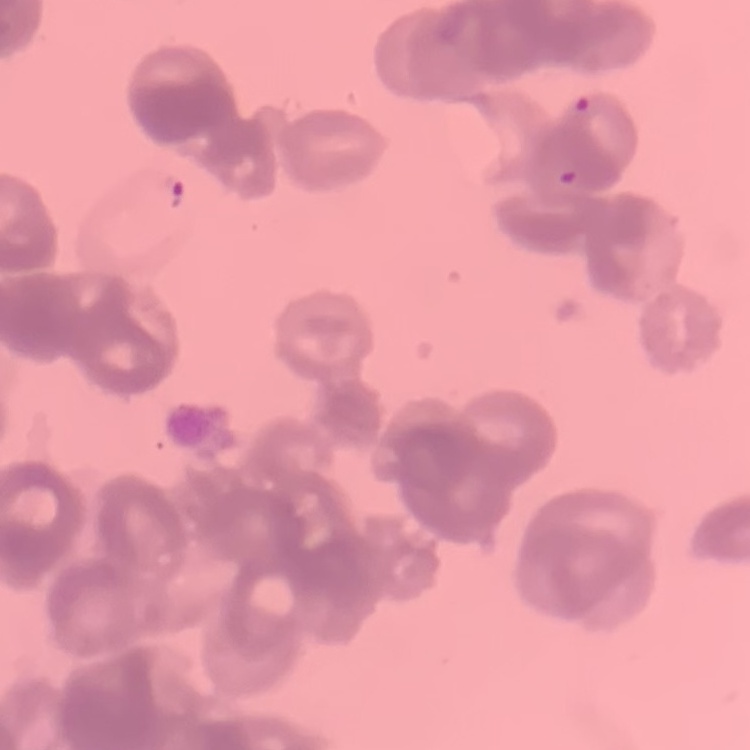
Summary:
  - Red blood cell morphology: rouleaux formation
  - Image type: square crop of a larger photomicrograph
  - Stain: Field's or Giemsa
  - Preparation: thin blood smear